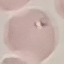

Summary:
  - Result: no malaria parasites seen
  - Image type: cell patch, automatically extracted from a larger field of view and resized to 64 × 64 pixels
  - Preparation: thin blood film
  - Capture: smartphone camera at the microscope eyepiece
  - Stain: Giemsa